Look for Plasmodium parasites.
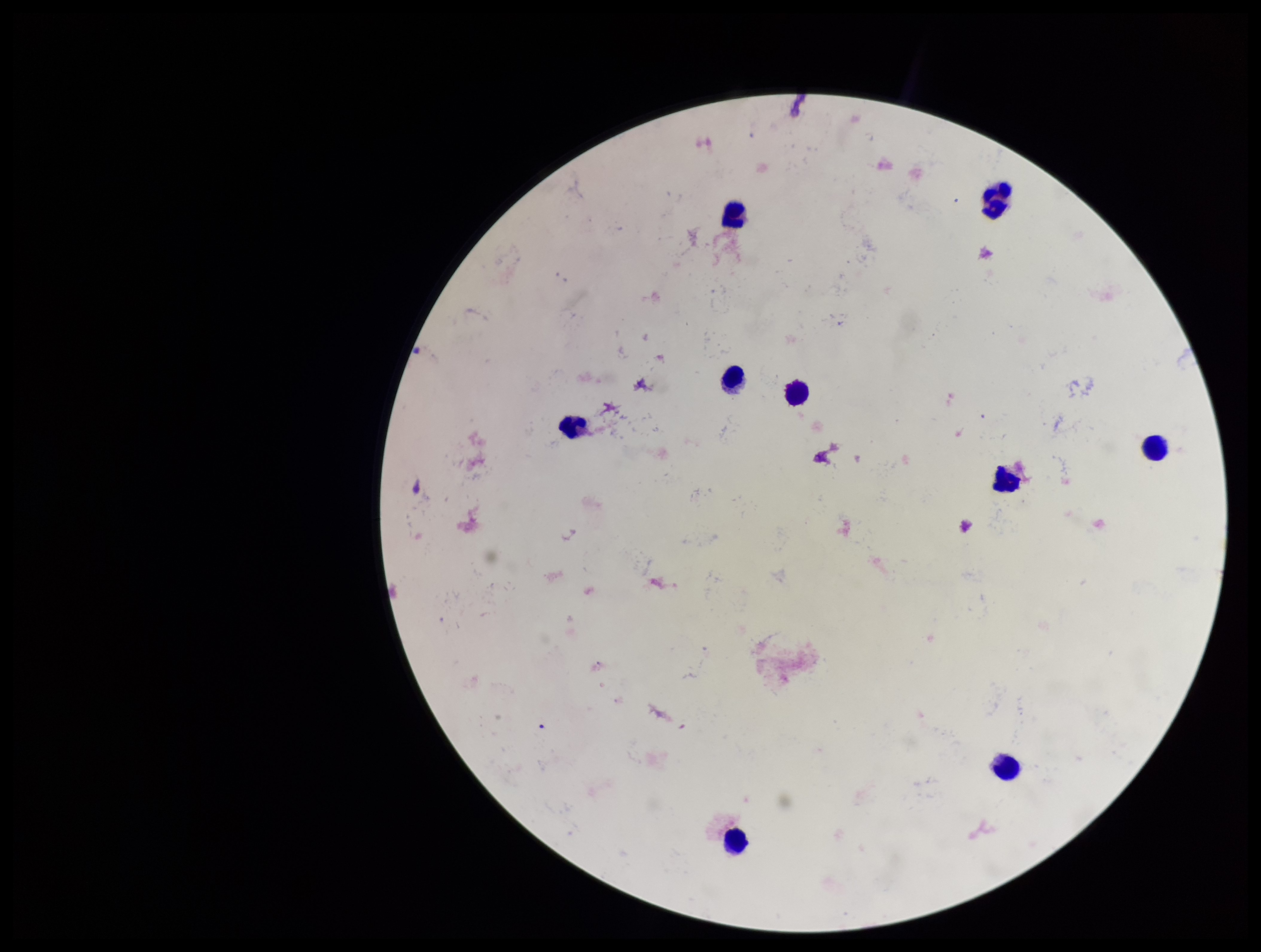

None seen.

Summary:
  - Image size: 1261×952 pixels
  - Stain: Giemsa
  - Patient malaria status: negative
  - Capture: smartphone photograph through the microscope eyepiece
  - Parasite count: 0
  - Field of view: one from this slide
  - Leukocyte count: 9
  - Preparation: thick smear